Assess this cell for malaria.
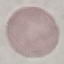

Uninfected.

Thin blood film. Acquired by smartphone through the microscope eyepiece. Automatically extracted cell patch, resized to 64 × 64 pixels. Giemsa-stained preparation.